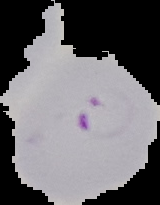 Image is 160×205 pixels. Cell region segmented out of the field of view; the surrounding area is masked to black. Result: malaria parasites identified. From a thin blood smear.